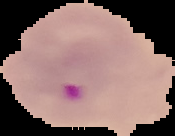

Image is 175×136 pixels. Result: malaria parasites identified. Cell region segmented out of the field of view; the surrounding area is masked to black. From a thin blood film.